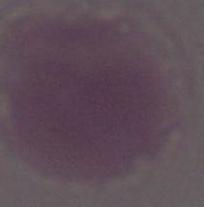
1000x magnification. Micrograph. An erythrocyte is shown.